Identify the parasite.
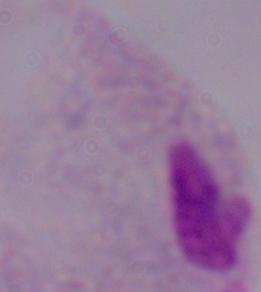
This is a trichomonad.

magnification = 1000x
modality = micrograph